Describe the morphology of the red blood cells.
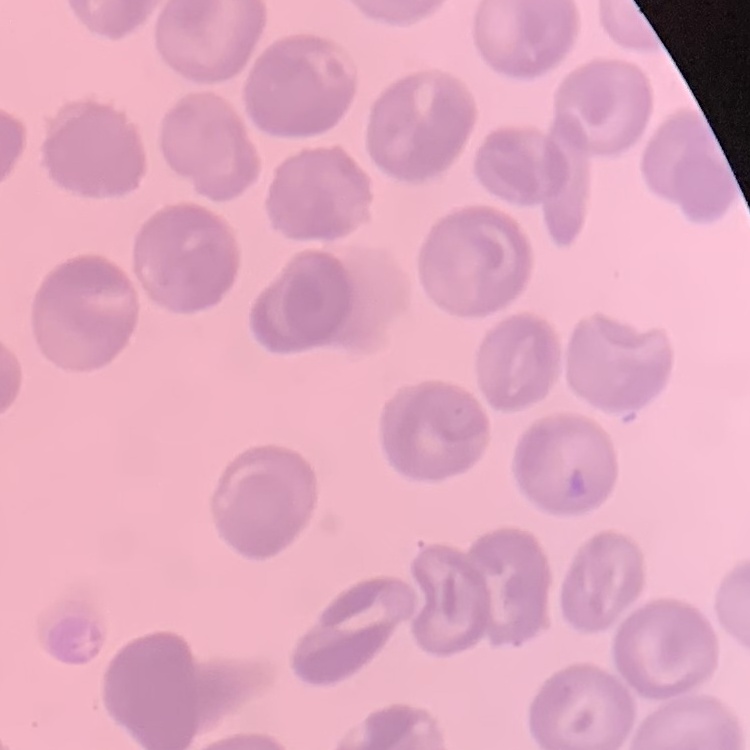

They show no rouleaux formation.

{
  "preparation": "thin blood film",
  "stain": "Field's or Giemsa",
  "image_type": "square crop of a larger photomicrograph"
}